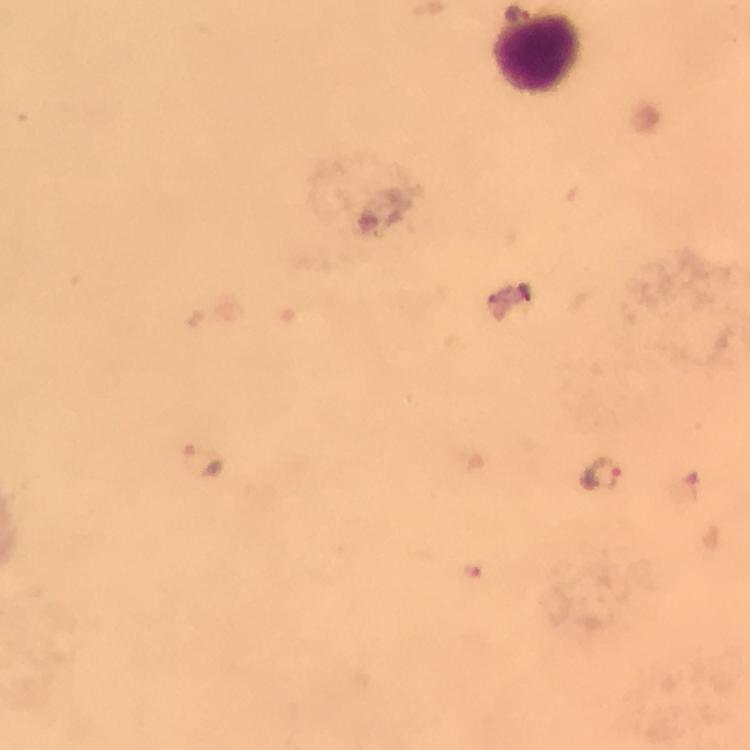 Approximate object centers, in pixels from the top-left corner. Malaria parasite locations: (x=517, y=12), (x=202, y=456), (x=598, y=473). Leukocyte locations: (x=536, y=53). From a diagnostic examination for malaria. Thick smear. Immersion oil was used. Giemsa stain. Image is 750×750 pixels. At 100x magnification. Photographed through the microscope with a smartphone camera. A crop from one field of view.